Classify this cell by malaria status.
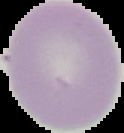
Uninfected.

{
  "image_type": "segmented cell region with the area outside set to black",
  "image_size": "124×133 pixels",
  "preparation": "thin blood smear"
}